Give the extent of all Plasmodium falciparum-infected red blood cells.
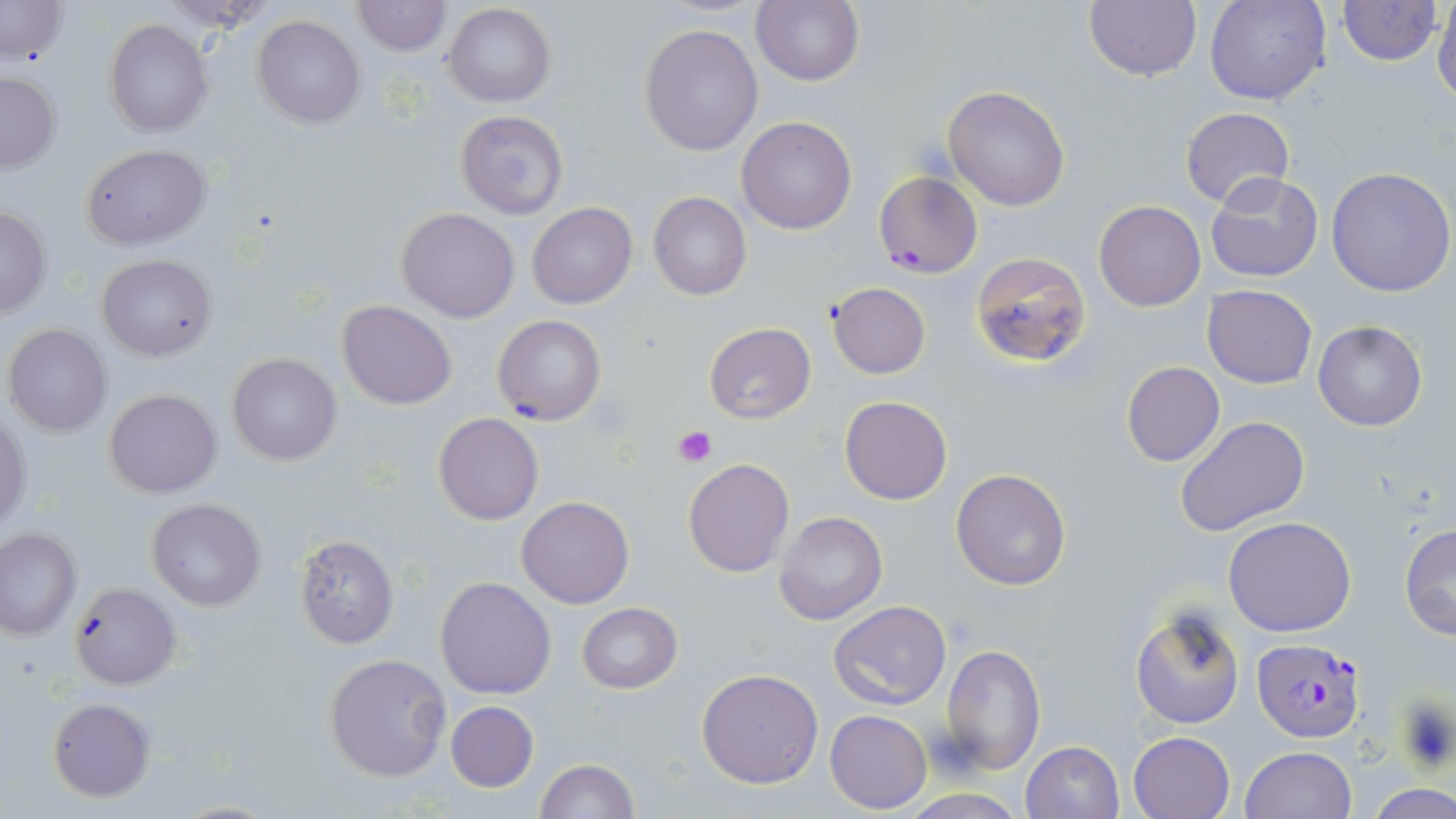

Approximate bounding boxes as (x1, y1, x2, y2) in pixels.
Plasmodium falciparum-infected red blood cells: (873, 171, 983, 278), (1252, 638, 1365, 743).

Summary:
  - Uninfected red blood cell locations: (0, 0, 69, 65), (752, 0, 865, 87), (1083, 0, 1202, 82), (1205, 0, 1330, 105), (1335, 0, 1442, 67), (1431, 0, 1456, 105), (352, 1, 450, 56), (444, 2, 555, 108), (252, 15, 367, 128), (103, 19, 213, 136), (639, 23, 765, 157), (0, 72, 61, 173), (942, 86, 1071, 212), (1180, 106, 1294, 211), (454, 109, 570, 222), (736, 116, 858, 235), (80, 143, 212, 250), (1326, 168, 1456, 298), (1206, 172, 1325, 285), (647, 191, 751, 301), (1094, 201, 1206, 313), (527, 203, 637, 310), (0, 205, 52, 320), (396, 207, 520, 322), (968, 251, 1094, 369), (96, 253, 217, 362), (826, 282, 931, 379), (1201, 285, 1317, 388), (335, 299, 459, 410), (492, 314, 606, 427), (1313, 320, 1427, 431), (4, 323, 112, 437), (703, 323, 817, 424), (227, 353, 343, 466), (1122, 361, 1224, 468), (103, 389, 222, 498), (839, 395, 951, 505), (1, 410, 31, 531), (1175, 416, 1311, 538), (434, 417, 544, 530), (683, 457, 795, 577), (951, 467, 1073, 591), (516, 495, 634, 608), (147, 499, 266, 610), (773, 511, 888, 627), (1223, 517, 1356, 638), (1399, 523, 1455, 641), (0, 527, 81, 639), (293, 535, 399, 648), (434, 575, 558, 699), (69, 579, 181, 688), (829, 600, 949, 710), (576, 603, 683, 694), (1129, 606, 1245, 729), (941, 644, 1044, 773), (323, 653, 453, 781), (696, 668, 823, 790), (47, 697, 156, 802), (444, 701, 538, 792), (824, 710, 931, 813), (1128, 730, 1235, 818), (1022, 739, 1125, 819), (1239, 746, 1358, 819), (534, 759, 638, 818), (1368, 784, 1456, 819)
  - Platelet locations: (674, 426, 716, 468), (1394, 694, 1455, 773)
  - Slide-level diagnosis: Plasmodium falciparum
  - Magnification: 1000x
  - Stain: May-Grünwald-Giemsa
  - Modality: light microscopy
  - Field of view: single
  - Preparation: thin blood film
  - Image size: 1456×819 pixels